Assess this cell for malaria.
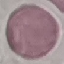

It is uninfected.

Summary:
  - Image type: cell patch, automatically extracted from a larger field of view and resized to 64 × 64 pixels
  - Capture: smartphone through the microscope eyepiece
  - Stain: Giemsa
  - Preparation: thin smear